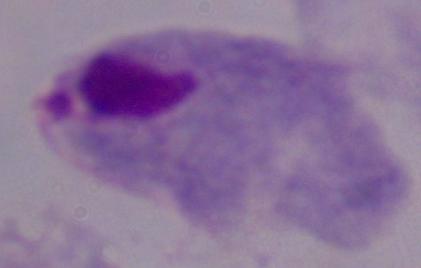

magnification = 1000x
identification = trichomonad
modality = photomicrograph